Report the malaria status of this cell.
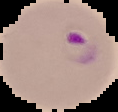
It is parasitized.

Image is 118×112 pixels. From a thin blood film. Cell region segmented out of the field of view; the surrounding area is masked to black.